Identify the blood parasite species.
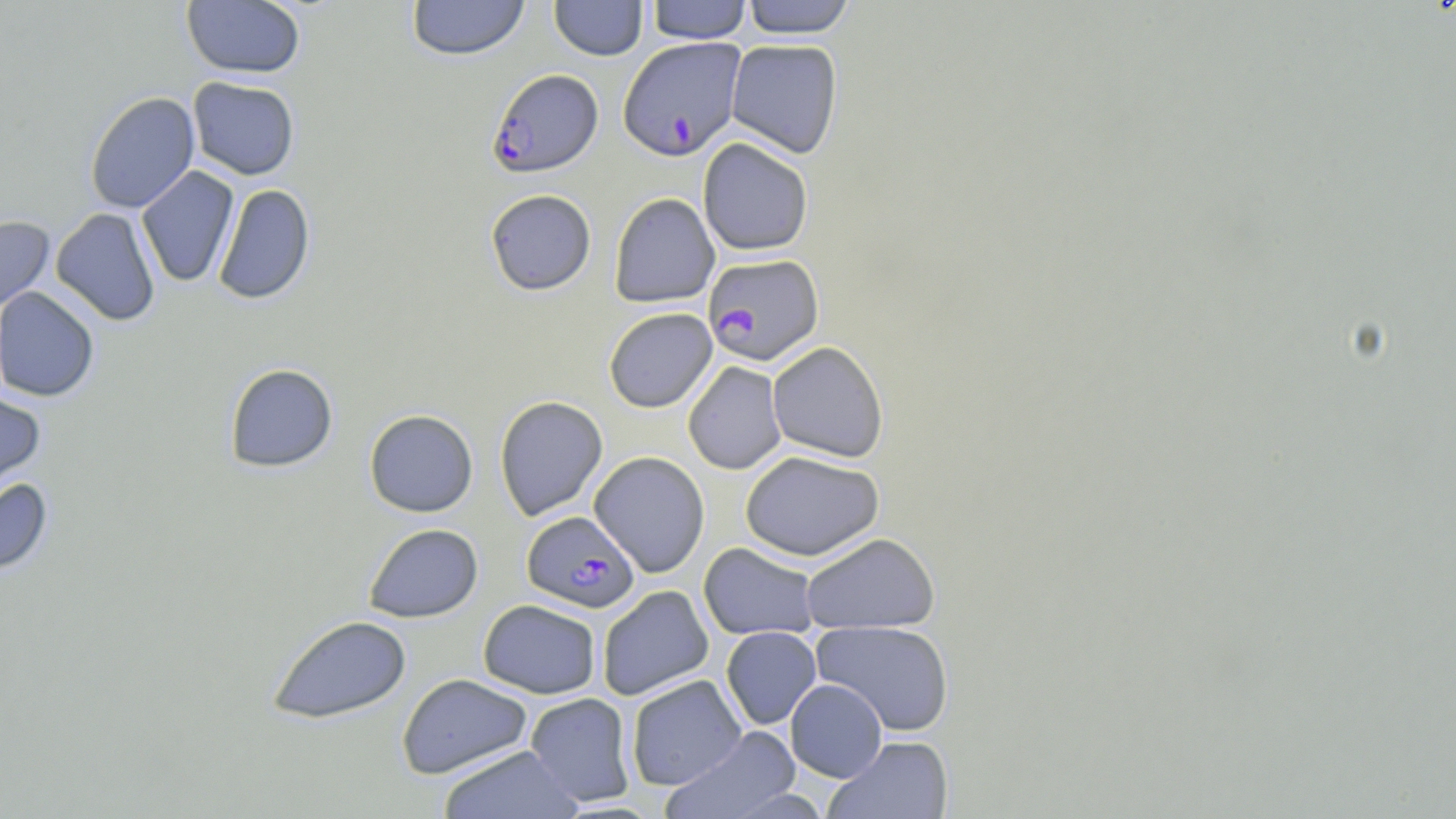
Plasmodium falciparum.

field of view = one of a larger specimen
uninfected red blood cell locations (subset) = approximate bounding boxes as (x1, y1, x2, y2) in pixels: (181, 0, 305, 79), (406, 0, 529, 61), (549, 0, 648, 61), (740, 0, 857, 38), (646, 1, 751, 44), (725, 39, 843, 158), (188, 76, 300, 180), (84, 91, 200, 214), (697, 137, 814, 256), (136, 166, 239, 287), (212, 184, 316, 305), (485, 189, 596, 295), (609, 192, 720, 308), (51, 207, 161, 326), (0, 216, 55, 313), (1, 285, 101, 403), (603, 308, 718, 413), (767, 341, 889, 463), (683, 361, 787, 475), (224, 363, 338, 472), (0, 388, 46, 496), (494, 395, 608, 521), (364, 409, 478, 517), (740, 450, 885, 561), (589, 451, 710, 577), (0, 478, 53, 574), (363, 523, 484, 623), (801, 532, 940, 634), (698, 542, 820, 641), (597, 585, 714, 701), (478, 599, 602, 699), (267, 614, 412, 724), (811, 620, 955, 736), (720, 626, 821, 729), (396, 673, 533, 779), (625, 674, 746, 791), (785, 679, 887, 782), (525, 693, 636, 807), (663, 725, 800, 819), (824, 736, 954, 819), (438, 745, 584, 819), (723, 788, 831, 818)
magnification = 1000x
image size = 1456×819 pixels
modality = light microscopy
stain = May-Grünwald-Giemsa
preparation = thin blood film
Plasmodium falciparum-infected red blood cell locations (subset) = approximate bounding boxes as (x1, y1, x2, y2) in pixels: (487, 69, 603, 177), (702, 253, 824, 365), (521, 510, 639, 613)